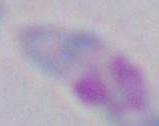
Summary:
  - Identification: Toxoplasma gondii
  - Magnification: 1000x
  - Modality: micrograph